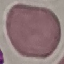 Malaria status: uninfected. Thin blood smear. Acquired by smartphone through the microscope eyepiece. Giemsa stain. Automatically extracted cell patch, resized to 64 × 64 pixels.